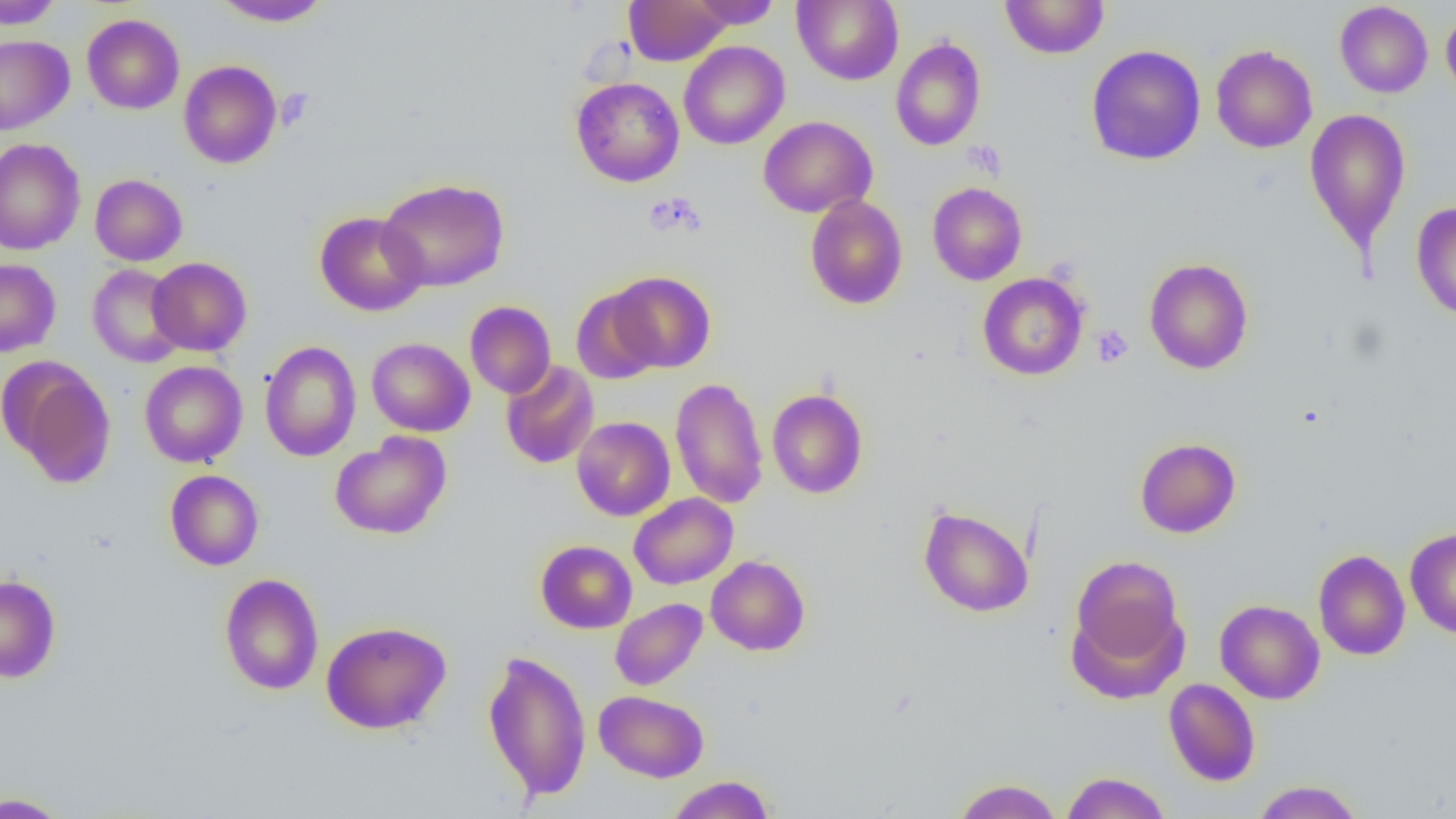

Summary:
  - Coordinate format: approximate bounding boxes as (x1,y1)-(x2,y2) corner pairs in pixels
  - Uninfected red blood cell locations: (0,0)-(64,29), (212,0)-(332,27), (624,0)-(731,66), (689,0)-(781,29), (793,0)-(903,85), (1000,0)-(1109,59), (1334,1)-(1433,98), (1441,9)-(1456,103), (82,14)-(184,114), (0,35)-(74,135), (890,36)-(986,151), (678,40)-(790,150), (1085,44)-(1206,165), (1211,45)-(1317,153), (179,60)-(283,168), (571,76)-(684,187), (1305,108)-(1411,251), (758,115)-(877,218), (0,139)-(85,255), (90,174)-(188,266), (377,178)-(509,292), (927,182)-(1027,285), (805,195)-(907,309), (1411,203)-(1456,320), (314,211)-(428,316), (148,257)-(252,356), (0,258)-(61,357), (1144,258)-(1254,374), (87,264)-(186,367), (609,271)-(715,373), (977,272)-(1089,380), (571,286)-(664,384), (465,301)-(556,398), (366,337)-(475,437), (260,341)-(361,461), (2,358)-(116,488), (139,360)-(247,468), (500,361)-(599,470), (670,377)-(768,509), (767,389)-(868,499), (572,416)-(675,521), (330,432)-(451,540), (1134,437)-(1241,538), (165,470)-(264,570), (629,493)-(738,589), (918,505)-(1034,617), (1405,528)-(1456,638), (535,540)-(637,633), (1313,550)-(1410,661), (706,555)-(810,656), (1068,555)-(1187,687), (220,573)-(323,695), (0,574)-(61,684), (610,598)-(708,690), (1215,599)-(1325,704), (320,620)-(451,735), (482,648)-(592,802), (1163,678)-(1260,786), (594,690)-(709,782), (1061,771)-(1171,819), (665,775)-(776,819), (953,778)-(1062,819), (1251,780)-(1365,819), (0,791)-(71,818)
  - Platelet locations: (964,141)-(1006,179), (643,193)-(705,238), (1091,325)-(1133,368)
  - Slide-level diagnosis: no evidence of blood parasites
  - Modality: light microscopy
  - Preparation: thin blood smear
  - Image size: 1456×819 pixels
  - Magnification: 1000x
  - Field of view: single